Classify this cell by malaria status.
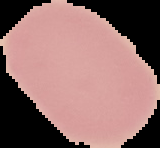

Uninfected.

From a thin blood film. Image is 160×148 pixels. Cell region segmented out of the field of view; the surrounding area is masked to black.